Name the parasite shown.
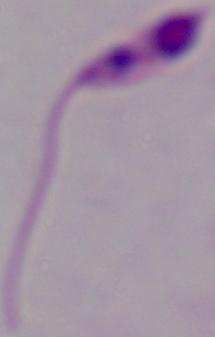
This is Leishmania.

1000x magnification. Photomicrograph.